Outline each uninfected red blood cell.
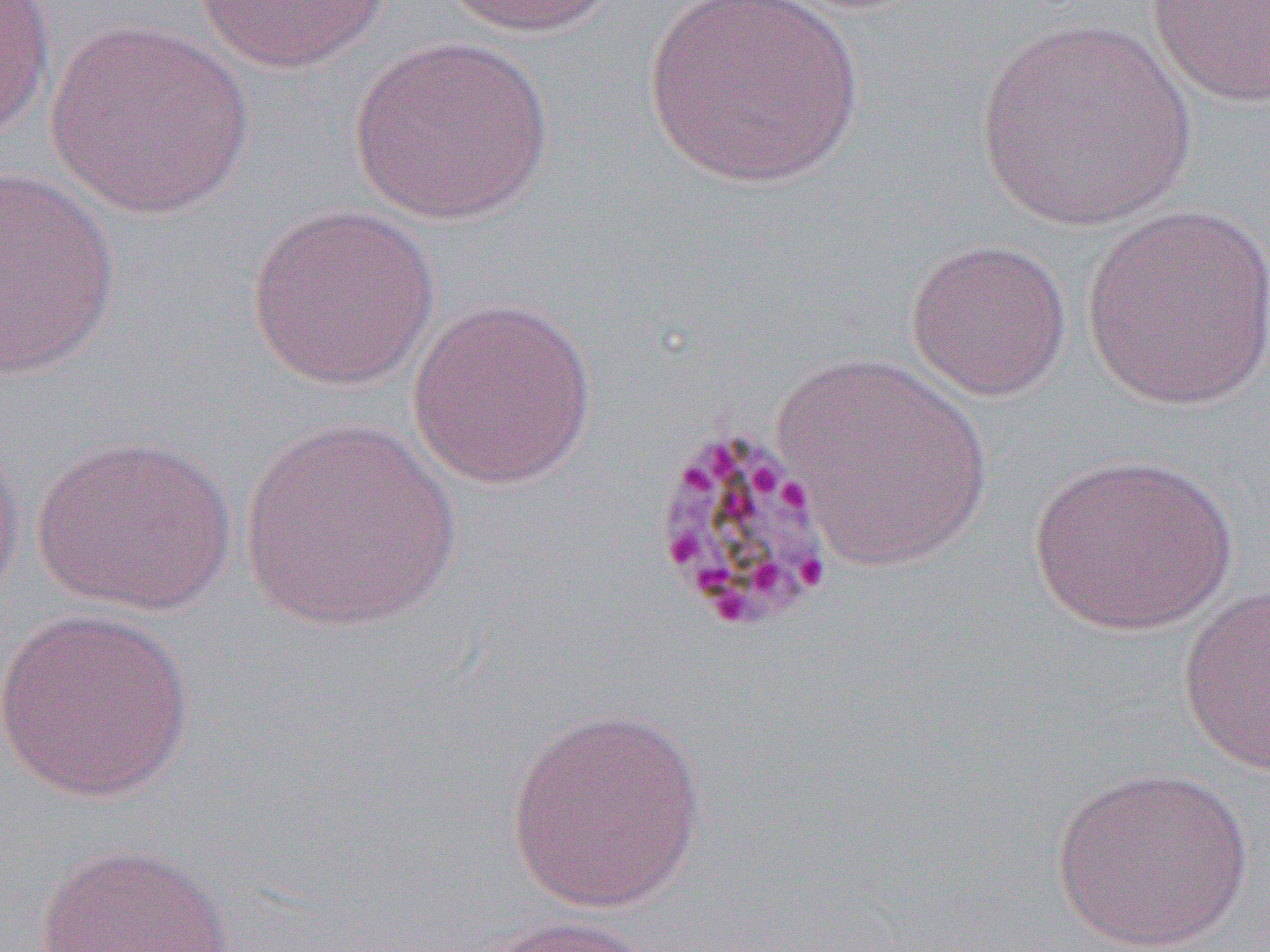

Approximate bounding boxes as (x1, y1, x2, y2) in pixels.
Uninfected red blood cells: (0, 0, 56, 142), (194, 0, 391, 73), (435, 0, 623, 38), (643, 0, 865, 189), (1146, 0, 1270, 108), (975, 18, 1196, 231), (43, 21, 256, 220), (347, 36, 555, 225), (0, 165, 121, 378), (1080, 202, 1270, 412), (245, 204, 440, 390), (904, 237, 1073, 403), (406, 295, 598, 490), (772, 353, 993, 573), (241, 416, 462, 632), (0, 427, 25, 614), (30, 435, 239, 615), (1028, 452, 1237, 637), (1177, 584, 1270, 776), (0, 607, 196, 803), (506, 705, 709, 915), (1051, 767, 1254, 950), (34, 843, 236, 952), (472, 914, 660, 952).

Slide-level diagnosis: Plasmodium malariae. 1000x magnification. Thin blood film. Light microscopy. Image is 1270×952 pixels. Single field of view.